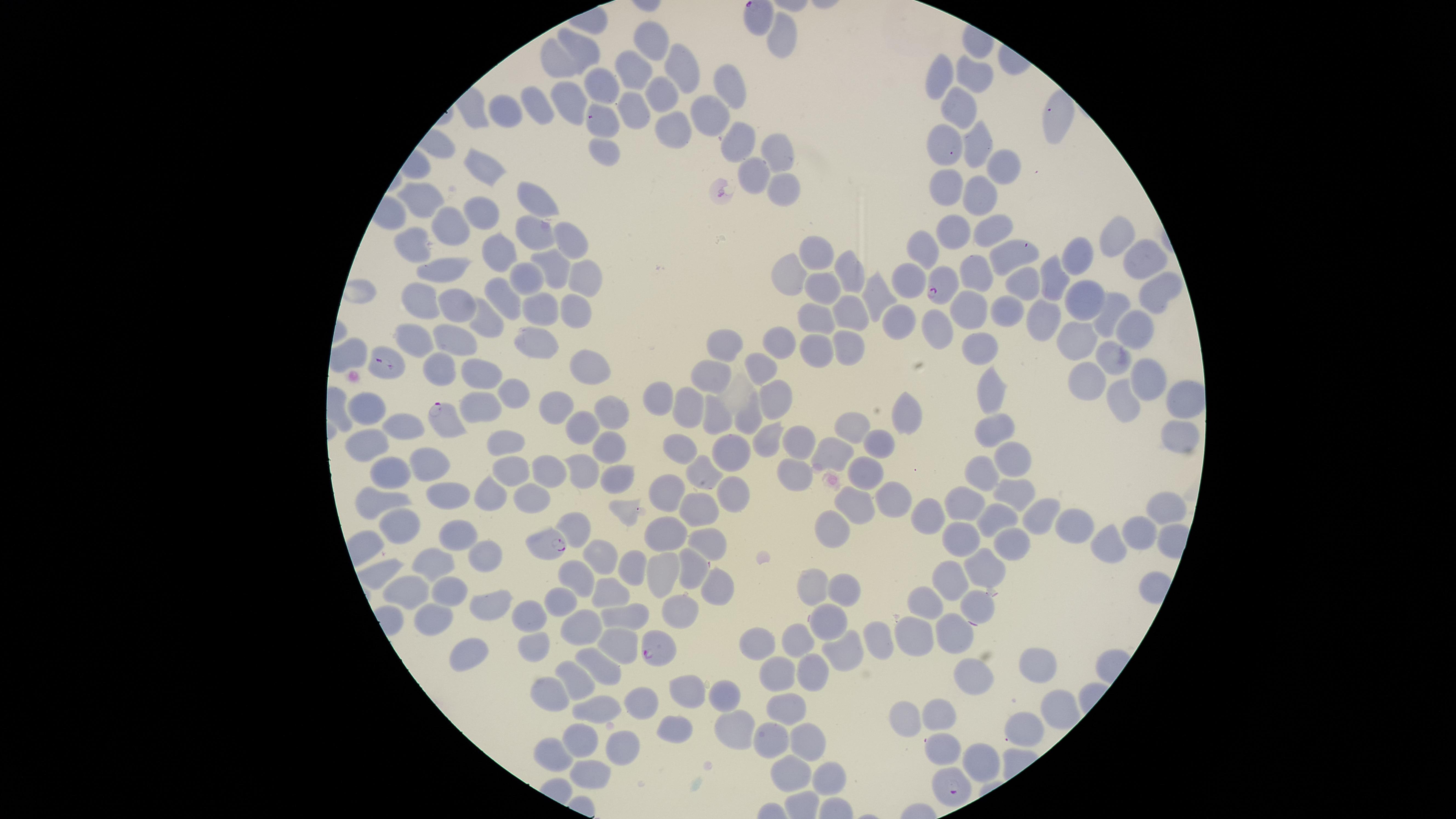

Approximate marker points as {x, y} in pixels.
Summary:
  - Uninfected RBCs: {785, 36}, {654, 40}, {576, 45}, {555, 64}, {638, 70}, {680, 70}, {978, 71}, {938, 72}, {595, 86}, {661, 88}, {729, 88}, {574, 102}, {960, 103}, {539, 104}, {635, 107}, {509, 108}, {1059, 113}, {710, 115}, {602, 125}, {670, 126}, {734, 137}, {982, 140}, {772, 144}, {943, 144}, {604, 149}, {1000, 162}, {479, 164}, {745, 167}, {779, 181}, {948, 185}, {531, 191}, {980, 194}, {416, 200}, {469, 211}, {991, 221}, {443, 223}, {568, 223}, {955, 227}, {533, 232}, {412, 238}, {1115, 240}, {929, 244}, {1010, 254}, {818, 255}, {494, 256}, {1076, 258}, {1136, 260}, {548, 266}, {973, 270}, {445, 271}, {572, 272}, {790, 274}, {529, 277}, {853, 277}, {909, 278}, {1053, 280}, {1021, 283}, {829, 286}, {502, 292}, {1154, 292}, {876, 295}, {421, 298}, {1083, 298}, {542, 301}, {453, 303}, {969, 305}, {567, 306}, {852, 306}, {1005, 308}, {1109, 309}, {813, 316}, {1046, 316}, {484, 321}, {900, 322}, {937, 328}, {1135, 329}, {1072, 335}, {539, 336}, {420, 337}, {453, 337}, {774, 339}, {979, 341}, {726, 342}, {842, 342}, {814, 344}, {1111, 352}, {583, 364}, {754, 364}, {478, 372}, {442, 373}, {703, 376}, {1143, 376}, {1084, 379}, {995, 385}, {513, 392}, {777, 396}, {657, 398}, {1181, 400}, {368, 402}, {692, 403}, {1121, 404}, {554, 406}, {478, 407}, {609, 407}, {910, 411}, {750, 414}, {709, 417}, {855, 417}, {395, 420}, {581, 425}, {994, 427}, {1173, 427}, {762, 437}, {786, 438}, {362, 439}, {505, 441}, {878, 445}, {611, 446}, {727, 446}, {830, 448}, {681, 449}, {426, 458}, {1010, 460}, {979, 466}, {786, 468}, {510, 469}, {390, 470}, {586, 470}, {862, 470}, {546, 471}, {701, 472}, {618, 477}, {614, 478}, {668, 487}, {724, 489}, {490, 490}, {447, 492}, {533, 492}, {1015, 494}, {890, 495}, {375, 496}, {850, 503}, {693, 504}, {967, 504}, {1155, 507}, {929, 510}, {1041, 511}, {997, 515}, {397, 520}, {1075, 520}, {664, 529}, {1132, 531}, {460, 532}, {829, 532}, {703, 535}, {960, 538}, {1006, 542}, {1108, 545}, {485, 549}, {599, 550}, {429, 558}, {686, 564}, {629, 567}, {984, 569}, {377, 571}, {657, 574}, {578, 576}, {951, 580}, {407, 583}, {840, 584}, {812, 585}, {712, 587}, {605, 590}, {449, 591}, {922, 598}, {560, 601}, {487, 602}, {972, 607}, {680, 610}, {438, 614}, {631, 614}, {533, 615}, {828, 621}, {578, 625}, {950, 627}, {913, 632}, {799, 638}, {756, 640}, {876, 640}, {530, 641}, {620, 642}, {837, 643}, {467, 649}, {1041, 662}, {774, 667}, {605, 669}, {812, 669}, {576, 673}, {973, 674}, {686, 685}, {721, 691}, {552, 692}, {638, 702}, {780, 711}, {598, 712}, {942, 713}, {1045, 714}, {909, 715}, {737, 720}, {675, 728}, {1024, 731}, {764, 736}, {581, 738}, {807, 741}, {622, 746}, {938, 746}, {547, 756}, {975, 758}, {785, 769}, {592, 775}, {830, 775}
  - Parasitized RBCs: {941, 286}, {387, 365}, {445, 421}, {548, 548}, {653, 650}, {946, 786}
  - Image size: 1456×819 pixels
  - Field of view: single
  - Stain: Giemsa
  - Capture: smartphone photograph through the microscope eyepiece
  - Species: Plasmodium falciparum
  - Preparation: thin blood film
  - Visible region: circular
  - Presence: malaria parasites detected